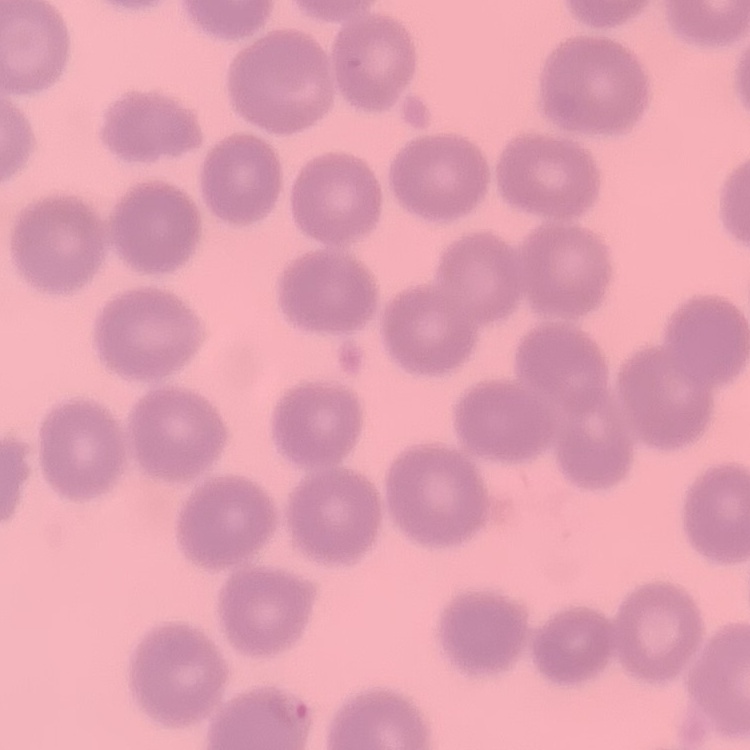
The erythrocytes exhibit no rouleaux formation. Stained with either Field's or Giemsa. Thin blood film. Square crop of a larger photomicrograph.